Give the position of every malaria parasite and every leukocyte.
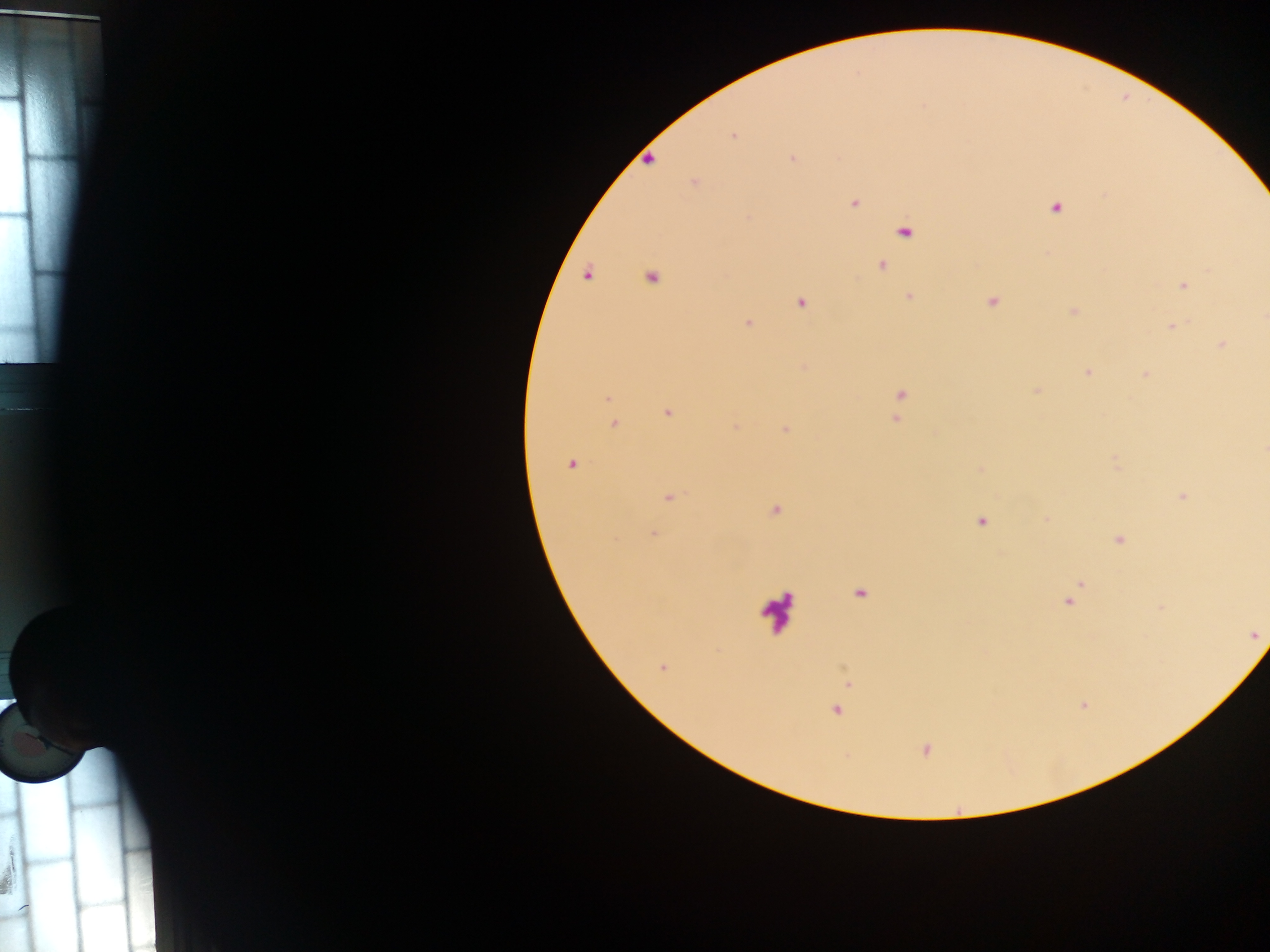
Approximate centers as [x, y] in pixels.
Malaria parasites: [732, 135], [650, 159], [792, 159], [693, 182], [854, 203], [1056, 208], [904, 233], [883, 266], [1209, 270], [587, 275], [651, 277], [1183, 286], [909, 295], [993, 301], [801, 303], [1073, 311], [748, 323], [1171, 327], [1222, 345], [1088, 372], [1145, 374], [900, 393], [607, 398], [669, 412], [895, 418], [614, 423], [786, 430], [1264, 450], [571, 464], [979, 469], [1182, 496], [669, 498], [775, 509], [980, 521], [654, 534], [1119, 540], [860, 594], [1068, 601], [662, 666], [836, 710], [926, 749].
Leukocytes: [775, 611].

Collected in Ghana. Mobile-phone photograph taken through the microscope. Thick blood smear. One field of view. Image is 1270×952 pixels.